Locate every blood parasite and identify its species.
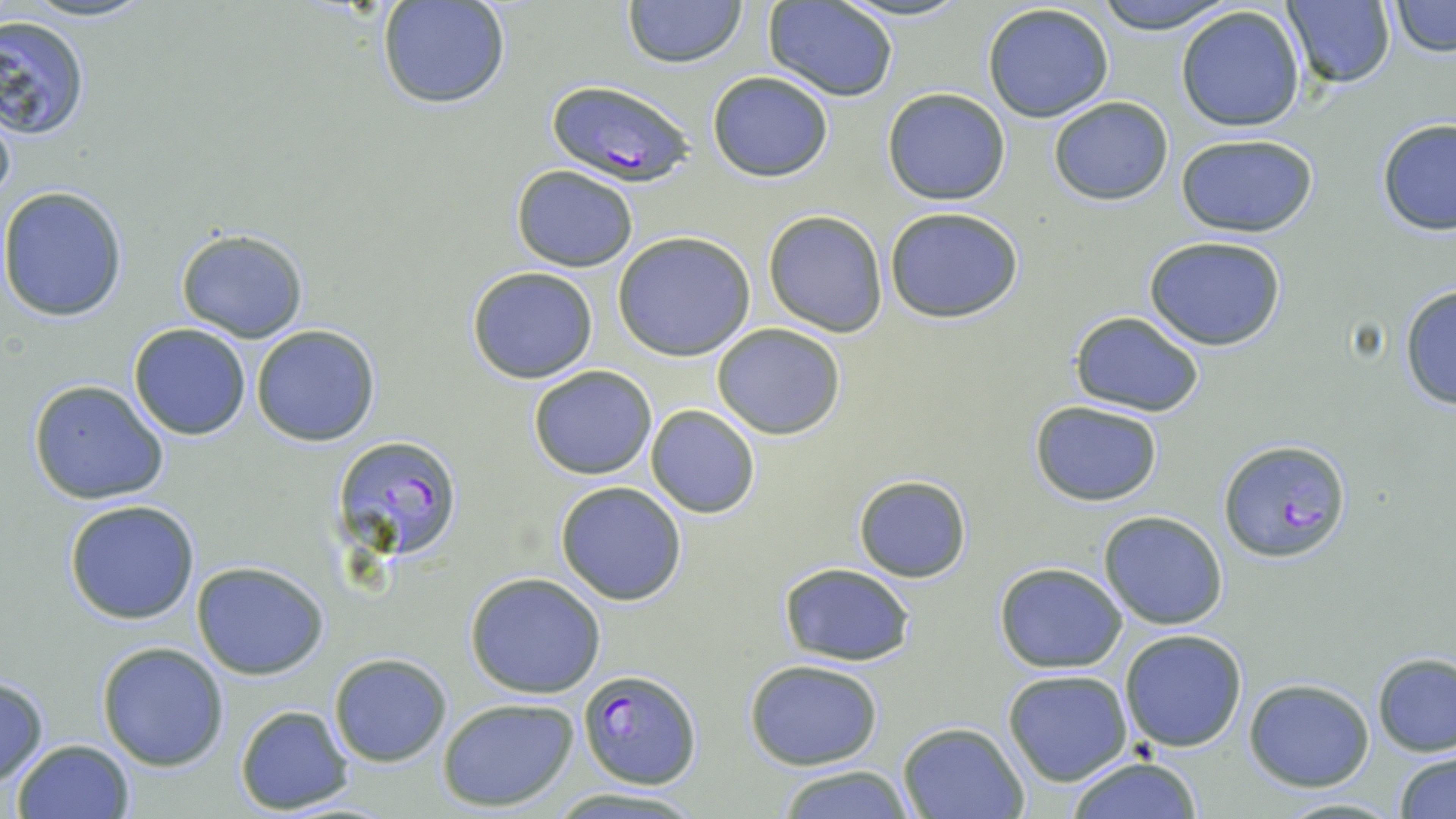

Approximate bounding boxes as named x1/y1/x2/y2 corners in pixels.
Plasmodium falciparum-infected red blood cells: (x1=545, y1=79, x2=696, y2=185), (x1=331, y1=432, x2=463, y2=560), (x1=1220, y1=436, x2=1351, y2=563), (x1=578, y1=668, x2=701, y2=790).
No Plasmodium ovale, Plasmodium malariae, Plasmodium vivax, Babesia divergens, or Trypanosoma brucei observed.

Summary:
  - Uninfected red blood cell locations: (x1=14, y1=0, x2=162, y2=24), (x1=621, y1=0, x2=748, y2=69), (x1=832, y1=0, x2=973, y2=23), (x1=1087, y1=0, x2=1237, y2=31), (x1=1282, y1=0, x2=1397, y2=90), (x1=377, y1=1, x2=513, y2=111), (x1=763, y1=1, x2=898, y2=100), (x1=1387, y1=2, x2=1454, y2=57), (x1=982, y1=3, x2=1115, y2=122), (x1=1175, y1=4, x2=1308, y2=133), (x1=0, y1=15, x2=90, y2=139), (x1=706, y1=71, x2=835, y2=183), (x1=882, y1=88, x2=1012, y2=205), (x1=1046, y1=96, x2=1174, y2=206), (x1=0, y1=97, x2=16, y2=220), (x1=1375, y1=118, x2=1456, y2=236), (x1=1175, y1=132, x2=1319, y2=237), (x1=510, y1=164, x2=639, y2=272), (x1=0, y1=185, x2=129, y2=322), (x1=882, y1=204, x2=1025, y2=323), (x1=763, y1=209, x2=890, y2=337), (x1=174, y1=227, x2=308, y2=344), (x1=612, y1=231, x2=756, y2=360), (x1=1145, y1=237, x2=1287, y2=351), (x1=465, y1=266, x2=599, y2=385), (x1=1398, y1=284, x2=1456, y2=411), (x1=1069, y1=311, x2=1206, y2=417), (x1=129, y1=323, x2=253, y2=440), (x1=712, y1=323, x2=846, y2=439), (x1=252, y1=325, x2=380, y2=447), (x1=527, y1=365, x2=658, y2=479), (x1=26, y1=379, x2=171, y2=504), (x1=1028, y1=400, x2=1166, y2=507), (x1=645, y1=404, x2=760, y2=518), (x1=852, y1=474, x2=972, y2=583), (x1=554, y1=480, x2=688, y2=606), (x1=62, y1=498, x2=202, y2=624), (x1=1098, y1=510, x2=1229, y2=629), (x1=993, y1=562, x2=1128, y2=673), (x1=191, y1=563, x2=331, y2=680), (x1=778, y1=563, x2=917, y2=666), (x1=464, y1=571, x2=608, y2=698), (x1=1119, y1=628, x2=1249, y2=752), (x1=97, y1=641, x2=229, y2=771), (x1=328, y1=653, x2=453, y2=768), (x1=1373, y1=654, x2=1456, y2=757), (x1=745, y1=659, x2=883, y2=770), (x1=1003, y1=671, x2=1132, y2=786), (x1=0, y1=675, x2=50, y2=788), (x1=1243, y1=678, x2=1375, y2=791), (x1=438, y1=696, x2=579, y2=812), (x1=235, y1=705, x2=355, y2=813), (x1=897, y1=722, x2=1027, y2=818), (x1=10, y1=739, x2=134, y2=819), (x1=1394, y1=751, x2=1456, y2=818), (x1=1065, y1=757, x2=1205, y2=818), (x1=772, y1=764, x2=915, y2=819), (x1=545, y1=787, x2=710, y2=817), (x1=1271, y1=795, x2=1404, y2=818)
  - Slide-level diagnosis: Plasmodium falciparum
  - Image size: 1456×819 pixels
  - Preparation: thin blood film
  - Modality: light microscopy
  - Magnification: 1000x
  - Stain: May-Grünwald-Giemsa
  - Field of view: one of a larger specimen